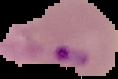

Summary:
  - Preparation: thin blood smear
  - Image size: 118×79 pixels
  - Image type: segmented cell region with the area outside set to black
  - Result: malaria parasites identified